Comment on the morphology of the red blood cells.
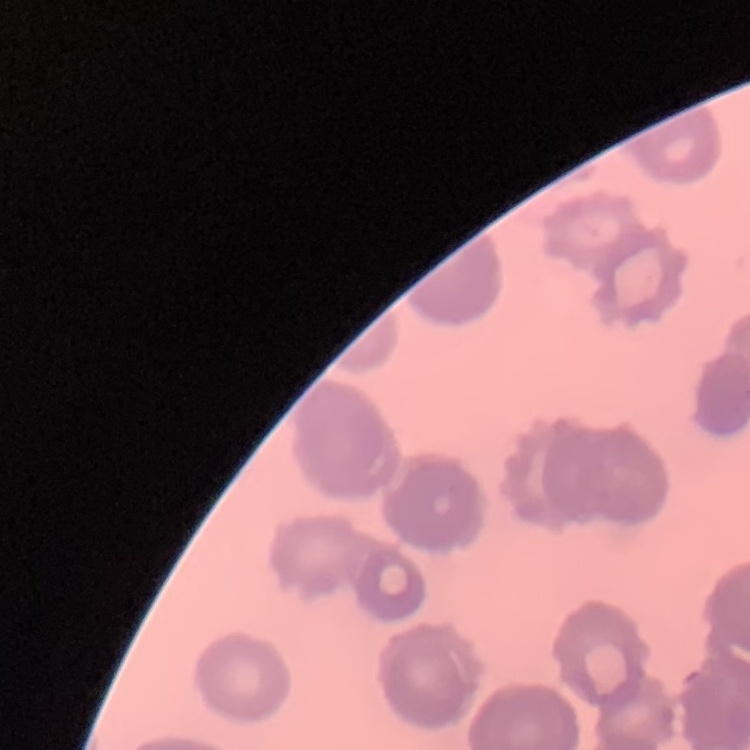
Rouleaux formation.

Thin peripheral smear. Stained with either Field's or Giemsa. One tile cut from a larger photomicrograph.